Classify this cell by malaria status.
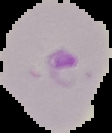
It is parasitized.

Summary:
  - Image type: segmented cell region on a black background
  - Preparation: thin blood film
  - Image size: 112×133 pixels